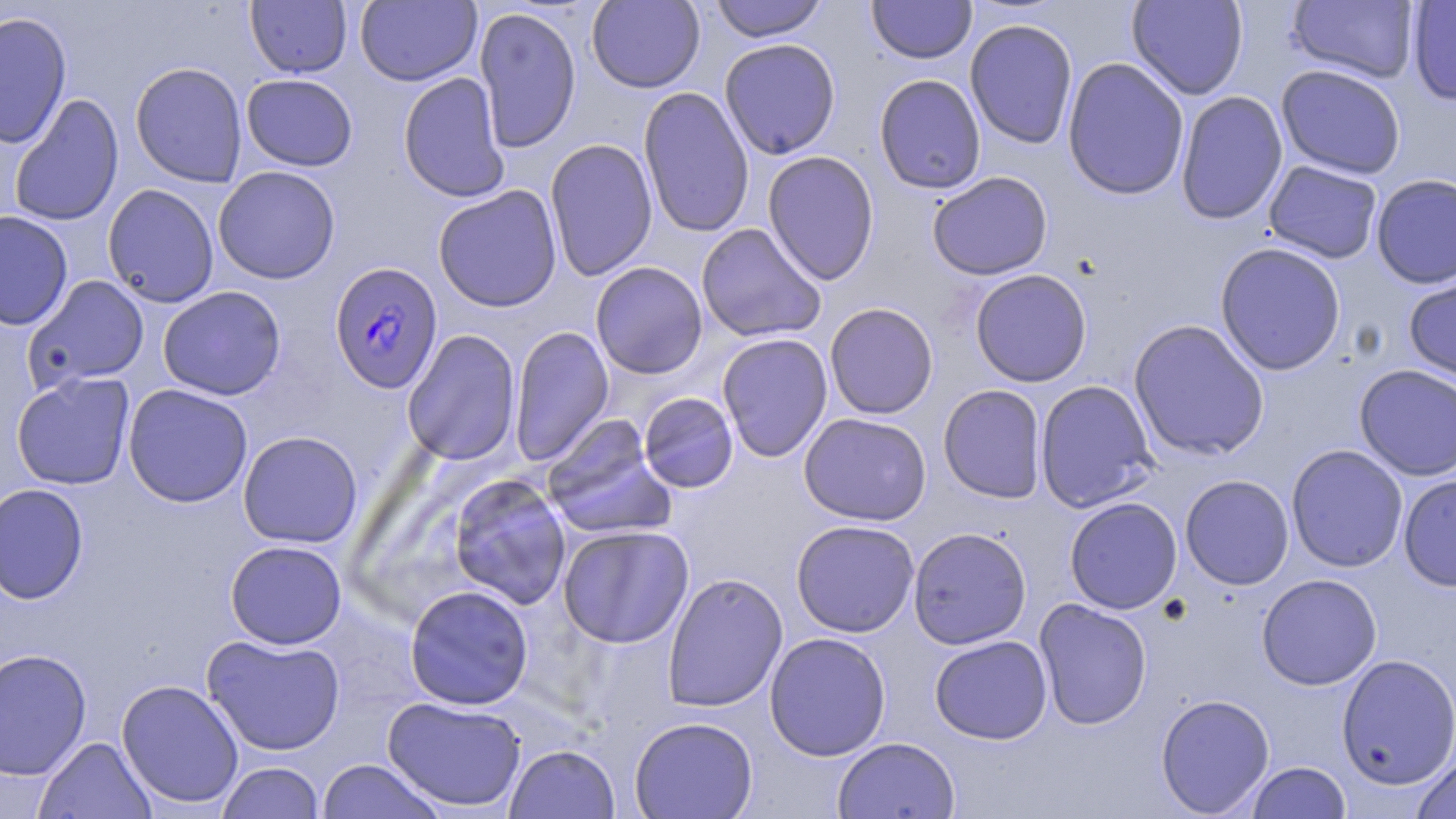

{
  "slide_level_diagnosis": "Plasmodium falciparum",
  "modality": "light microscopy",
  "magnification": "1000x",
  "image_size": "1456×819 pixels",
  "stain": "May-Grünwald-Giemsa",
  "uninfected_red_blood_cell_locations": "approximate bounding boxes as [x1, y1, x2, y2] in pixels: [355, 0, 481, 86], [587, 0, 705, 93], [709, 0, 828, 43], [867, 0, 976, 64], [1127, 0, 1248, 100], [1287, 0, 1421, 83], [245, 1, 352, 78], [1407, 1, 1456, 105], [474, 6, 582, 153], [0, 11, 72, 149], [964, 18, 1078, 150], [719, 38, 841, 159], [1062, 57, 1190, 201], [130, 62, 248, 188], [1276, 64, 1407, 179], [398, 72, 510, 203], [241, 73, 358, 171], [874, 73, 987, 195], [638, 87, 754, 238], [1175, 91, 1288, 225], [8, 94, 125, 226], [545, 138, 658, 281], [762, 150, 880, 285], [1263, 160, 1383, 264], [212, 166, 341, 284], [926, 171, 1053, 280], [1371, 173, 1456, 289], [102, 184, 219, 307], [433, 185, 563, 312], [0, 210, 73, 331], [696, 223, 826, 343], [1214, 242, 1346, 376], [590, 261, 708, 379], [1403, 268, 1456, 388], [969, 269, 1092, 387], [23, 275, 150, 393], [157, 285, 286, 400], [824, 302, 939, 419], [1128, 319, 1270, 461], [509, 324, 615, 466], [401, 330, 521, 465], [716, 332, 833, 462], [1354, 364, 1456, 481], [11, 372, 135, 490], [1035, 379, 1159, 513], [123, 384, 253, 508], [938, 384, 1048, 504], [638, 392, 739, 493], [798, 412, 932, 526], [541, 415, 676, 541], [238, 430, 362, 548], [1285, 445, 1408, 572], [448, 474, 572, 610], [1180, 474, 1294, 590], [1398, 474, 1456, 591], [0, 483, 89, 604], [1064, 497, 1183, 614], [791, 519, 919, 638], [557, 524, 694, 648], [907, 527, 1032, 649], [225, 540, 347, 649], [662, 573, 788, 712], [1256, 573, 1382, 690], [404, 585, 534, 710], [1034, 599, 1152, 730], [764, 632, 891, 760], [202, 634, 345, 756], [929, 635, 1052, 744], [0, 648, 92, 780], [1336, 654, 1456, 791], [116, 679, 244, 809], [1155, 693, 1275, 817], [382, 696, 527, 813], [629, 716, 758, 819], [33, 736, 156, 819], [832, 737, 960, 819], [504, 743, 620, 818], [1410, 752, 1456, 819], [316, 759, 445, 819], [215, 761, 325, 819], [1246, 761, 1351, 818]",
  "plasmodium_falciparum_infected_red_blood_cell_locations": "approximate bounding boxes as [x1, y1, x2, y2] in pixels: [329, 262, 443, 394]",
  "preparation": "thin blood film",
  "field_of_view": "single"
}